Classify this cell by malaria status.
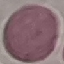

It is uninfected.

Photographed with a smartphone camera at the microscope eyepiece. Giemsa-stained preparation. Thin blood smear. Automatically extracted cell patch, resized to 64 × 64 pixels.